Find the cells and give the type of each one.
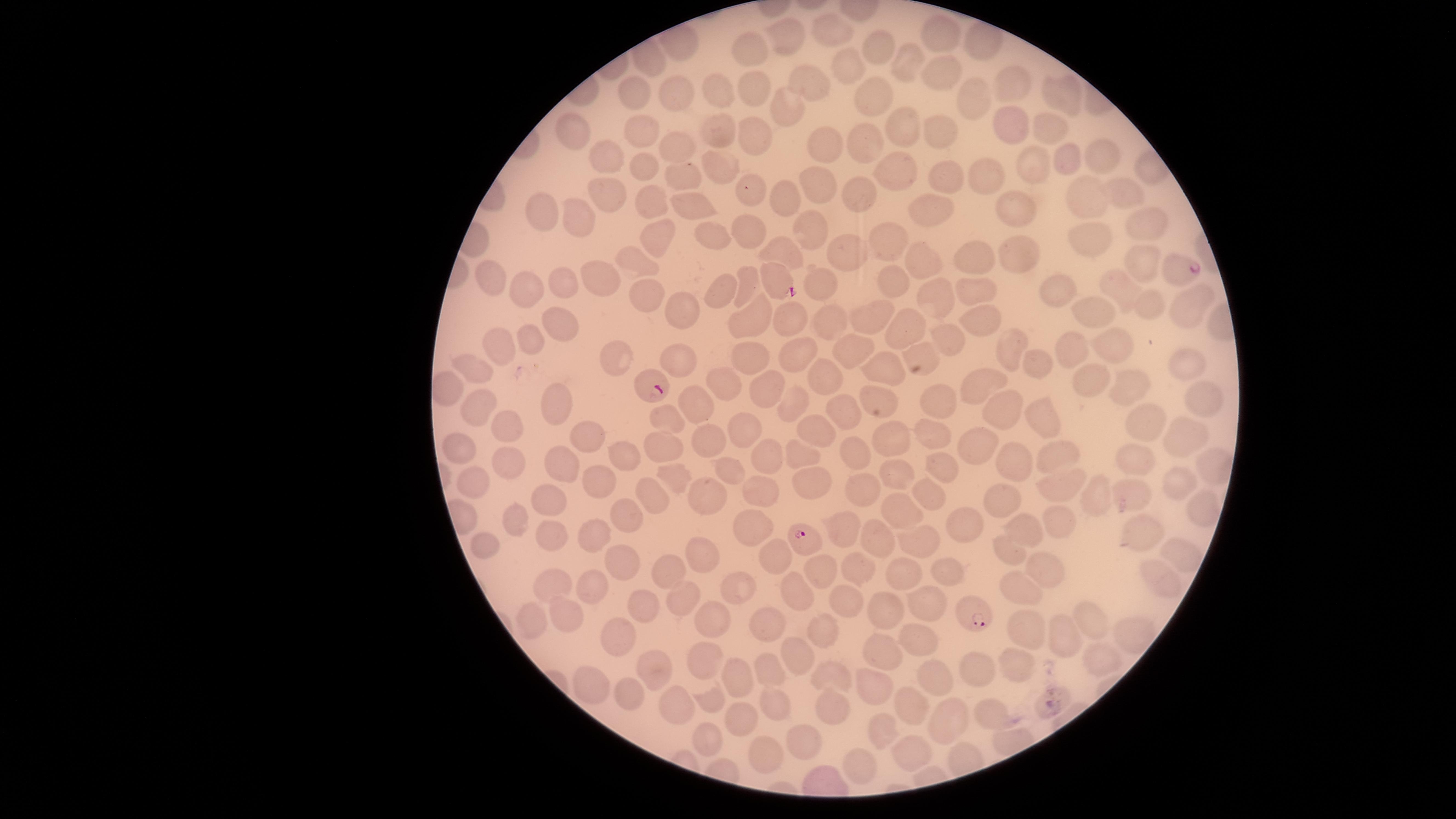

Approximate marker points as [x, y] in pixels.
Parasitized red blood cells: [1177, 268], [780, 280], [651, 382], [803, 537], [974, 614].
Uninfected red blood cells: [830, 29], [942, 29], [787, 37], [882, 46], [752, 49], [910, 60], [847, 69], [940, 73], [806, 81], [754, 84], [1007, 84], [718, 92], [1054, 95], [637, 96], [868, 96], [976, 98], [678, 99], [782, 112], [1007, 121], [900, 123], [1044, 125], [642, 128], [716, 129], [572, 131], [940, 132], [754, 136], [867, 140], [821, 143], [679, 148], [606, 155], [1106, 158], [1072, 160], [1034, 162], [644, 166], [725, 168], [895, 172], [684, 173], [946, 175], [983, 176], [754, 186], [819, 187], [1127, 187], [609, 192], [861, 194], [655, 197], [696, 197], [1086, 198], [785, 200], [1021, 205], [935, 212], [548, 213], [577, 221], [808, 224], [1152, 224], [751, 229], [657, 234], [712, 234], [1090, 238], [882, 242], [783, 251], [852, 251], [1018, 254], [975, 257], [639, 259], [1140, 259], [923, 263], [491, 275], [598, 276], [894, 276], [748, 281], [819, 283], [556, 284], [975, 284], [726, 287], [528, 288], [1126, 288], [1062, 289], [649, 292], [936, 294], [688, 305], [1145, 306], [1185, 306], [1098, 308], [875, 313], [785, 319], [823, 320], [982, 320], [557, 323], [748, 324], [905, 328], [531, 339], [946, 340], [497, 342], [1011, 345], [1113, 345], [858, 347], [1075, 349], [747, 351], [923, 353], [801, 354], [621, 356], [681, 360], [1182, 361], [1036, 363], [479, 366], [891, 368], [827, 378], [1092, 379], [1128, 380], [982, 381], [722, 382], [769, 383], [937, 402], [554, 403], [696, 407], [788, 407], [478, 411], [995, 411], [837, 412], [1041, 418], [667, 421], [1143, 422], [740, 426], [505, 428], [810, 429], [928, 434], [1177, 434], [892, 436], [581, 437], [707, 441], [977, 443], [458, 450], [662, 450], [798, 450], [855, 456], [1050, 456], [759, 458], [566, 460], [1013, 460], [624, 461], [1131, 461], [505, 462], [942, 462], [722, 469], [891, 473], [473, 479], [592, 479], [678, 480], [808, 481], [1174, 482], [1058, 487], [863, 489], [758, 490], [1002, 491], [1097, 492], [708, 493], [927, 493], [1128, 494], [652, 497], [548, 502], [1199, 508], [897, 510], [623, 515], [514, 518], [1057, 519], [958, 524], [843, 525], [747, 528], [1022, 530], [546, 531], [1130, 532], [595, 536], [916, 540], [482, 541], [876, 541], [1005, 550], [774, 552], [696, 553], [1173, 554], [618, 555], [818, 566], [1040, 567], [858, 569], [902, 571], [944, 573], [668, 574], [1157, 581], [548, 584], [593, 586], [1019, 588], [797, 591], [738, 592], [682, 599], [847, 602], [928, 603], [642, 607], [765, 613], [881, 613], [570, 617], [534, 619], [1090, 620], [712, 621], [819, 628], [1025, 633], [919, 635], [1062, 635], [621, 637], [794, 645], [877, 647], [706, 657], [1096, 659], [654, 663], [1016, 664], [977, 667], [769, 668], [830, 673], [931, 675], [743, 678], [871, 681], [584, 684], [628, 692], [704, 697], [669, 704], [776, 704], [837, 707], [913, 709], [988, 710], [952, 714], [742, 718], [878, 729], [705, 740], [806, 743], [911, 751], [768, 752], [863, 766].
No white blood cells identified.

Image is 1456×819 pixels. The visible region is circular. One field of view of the specimen. Thin blood film. Giemsa stain. Photographed with a smartphone camera through the microscope eyepiece. Species: Plasmodium falciparum.